Locate every Plasmodium parasite.
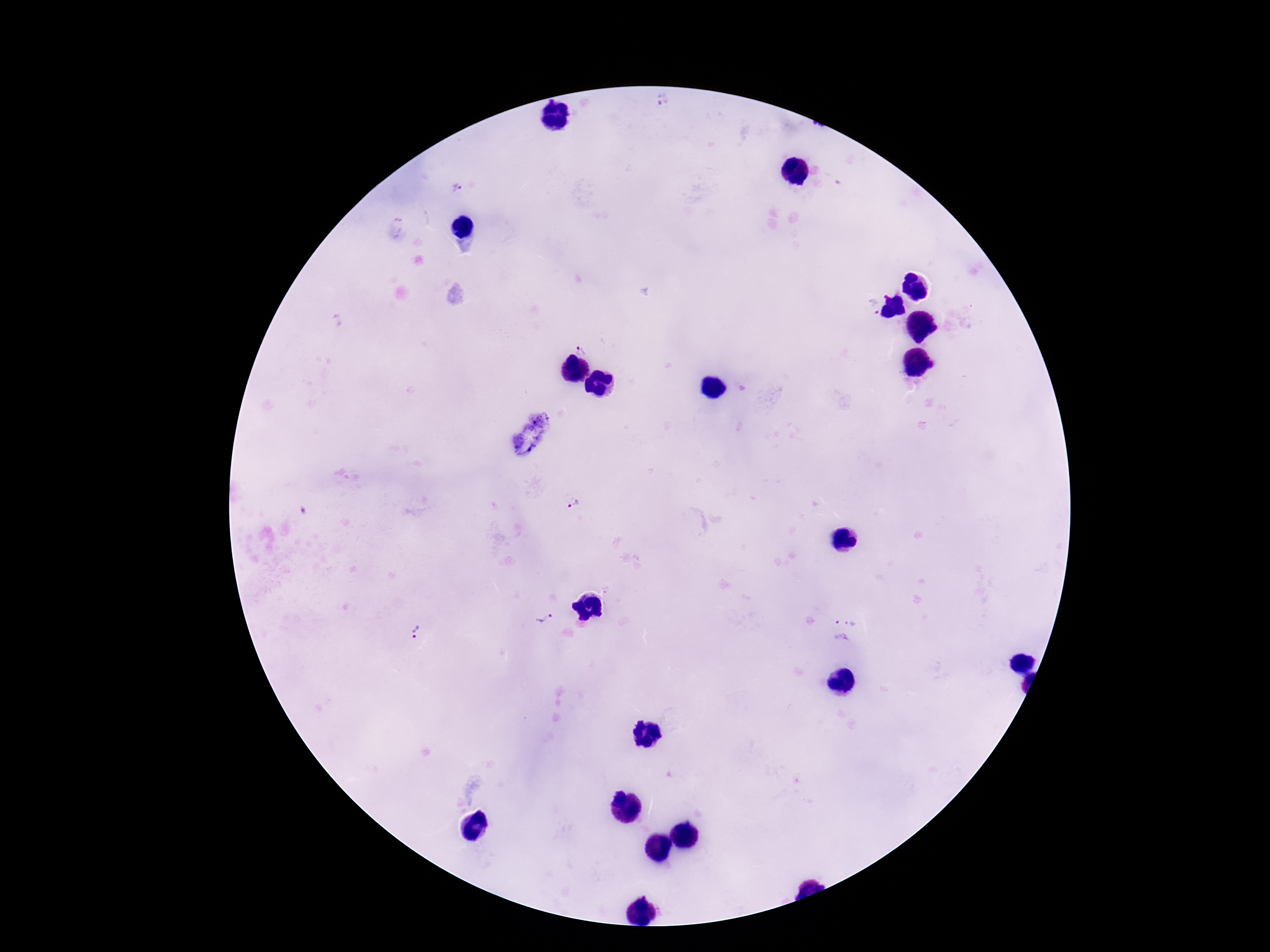
Approximate centers as [x, y] in pixels.
Plasmodium parasites: [667, 101], [457, 188], [870, 308], [581, 345], [574, 503], [846, 615], [543, 618], [415, 630].

field of view = single
magnification = 100x
stain = Giemsa
preparation = thick blood smear
patient malaria status = infected
image size = 1270×952 pixels
capture = smartphone camera through the microscope eyepiece